Assess the morphology of the red blood cells.
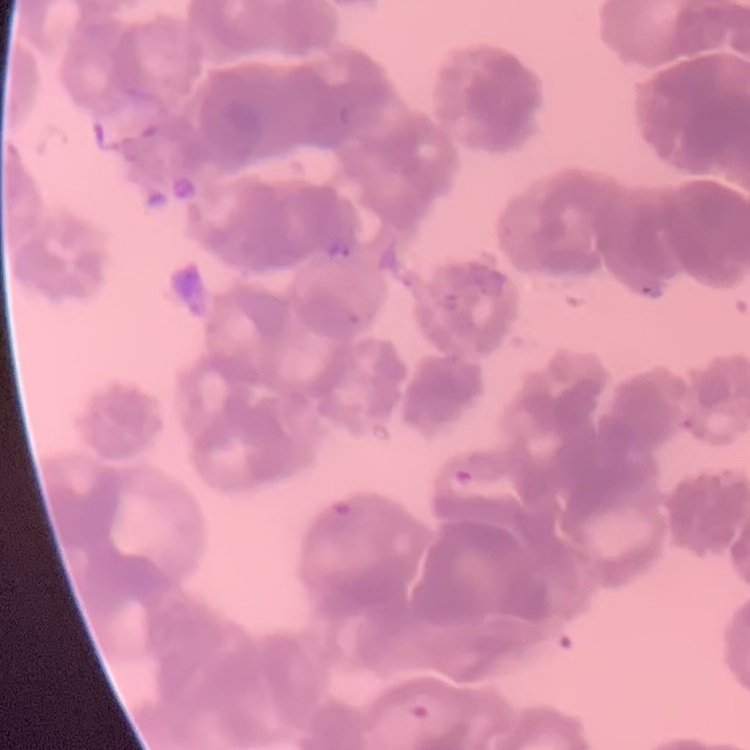
They show rouleaux formation.

Summary:
  - Preparation: thin blood film
  - Stain: Field's or Giemsa
  - Image type: square crop of a larger photomicrograph